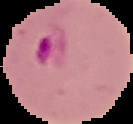
Summary:
  - Result: Plasmodium parasites detected
  - Image type: segmented cell region on a black background
  - Image size: 133×124 pixels
  - Preparation: thin blood smear